Assess this cell for malaria.
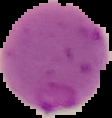
Parasitized.

From a thin blood film. Image is 112×118 pixels. Segmented cell region on a black background.